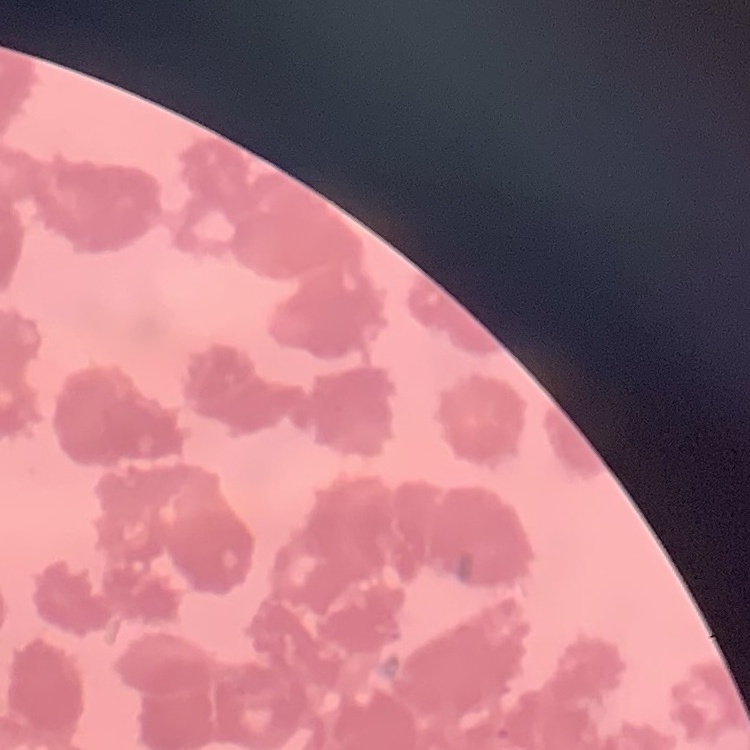
The erythrocytes show rouleaux formation. Square crop of a larger photomicrograph. Thin blood smear. Field's or Giemsa stain.